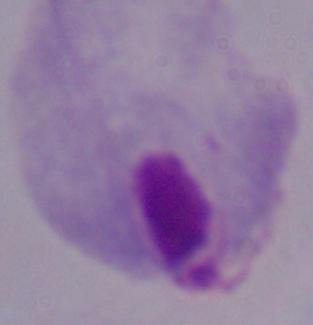

magnification = 1000x
identification = trichomonad
modality = micrograph